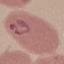
Summary:
  - Result: malaria parasites identified
  - Stain: Giemsa
  - Image type: cell patch, automatically extracted from a larger field of view and resized to 64 × 64 pixels
  - Capture: smartphone camera at the microscope eyepiece
  - Preparation: thin blood smear